Name the cell type shown.
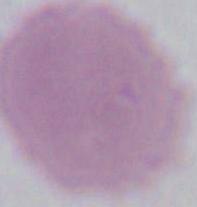
This is an erythrocyte.

Summary:
  - Magnification: 1000x
  - Modality: photomicrograph